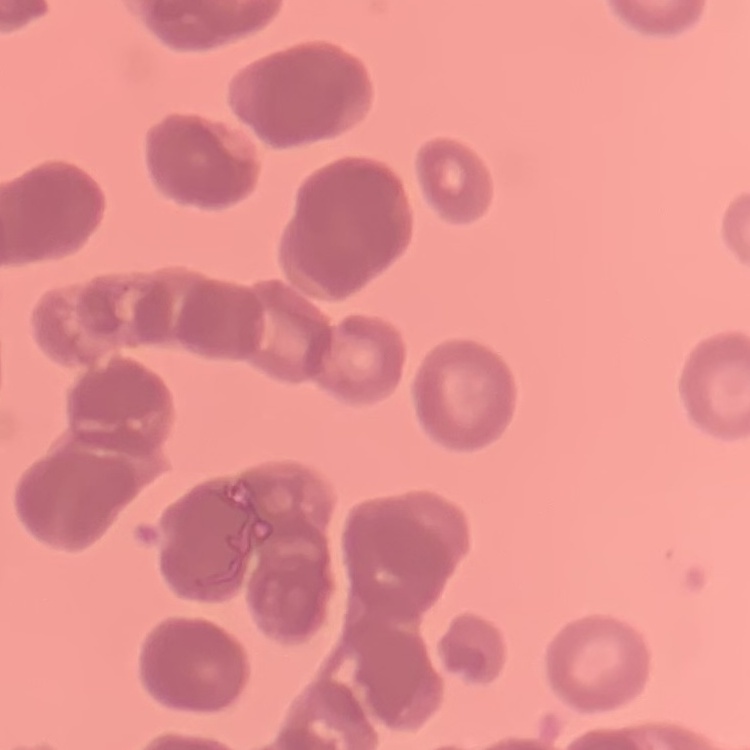
Summary:
  - Red blood cell morphology: rouleaux formation
  - Image type: square crop of a larger photomicrograph
  - Stain: Field's or Giemsa
  - Preparation: thin blood film